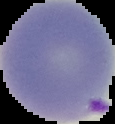
Summary:
  - Image type: segmented cell region with the area outside set to black
  - Image size: 115×124 pixels
  - Preparation: thin blood smear
  - Malaria status: parasitized